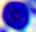 Captured at 400x magnification. Photomicrograph. A leukocyte is seen.